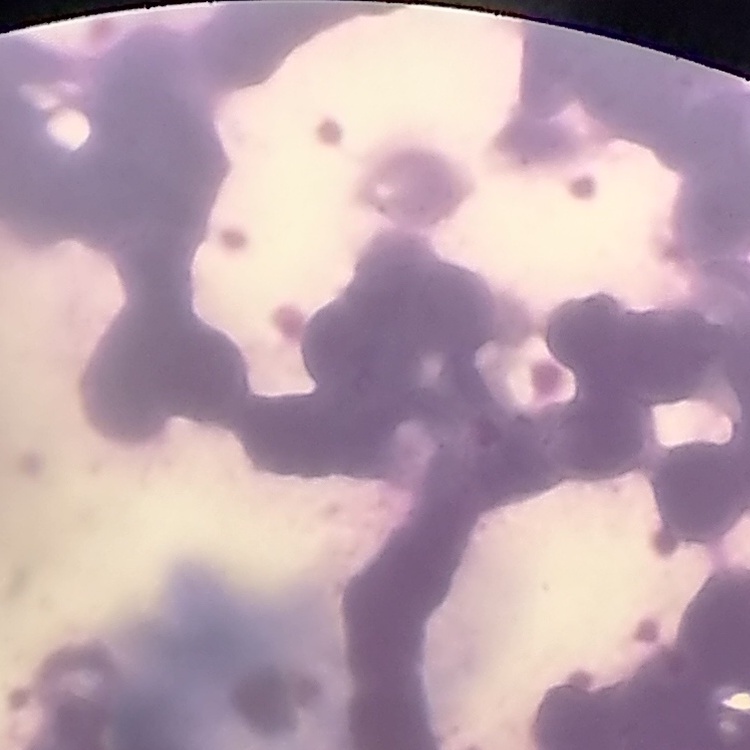

{
  "red_blood_cell_morphology": "rouleaux formation",
  "preparation": "thin blood smear",
  "image_type": "square crop of a larger photomicrograph",
  "stain": "Field's or Giemsa"
}